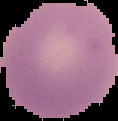 Cell region segmented out of the field of view; the surrounding area is masked to black. From a thin blood smear. Result: negative for malaria parasites. Image is 118×121 pixels.